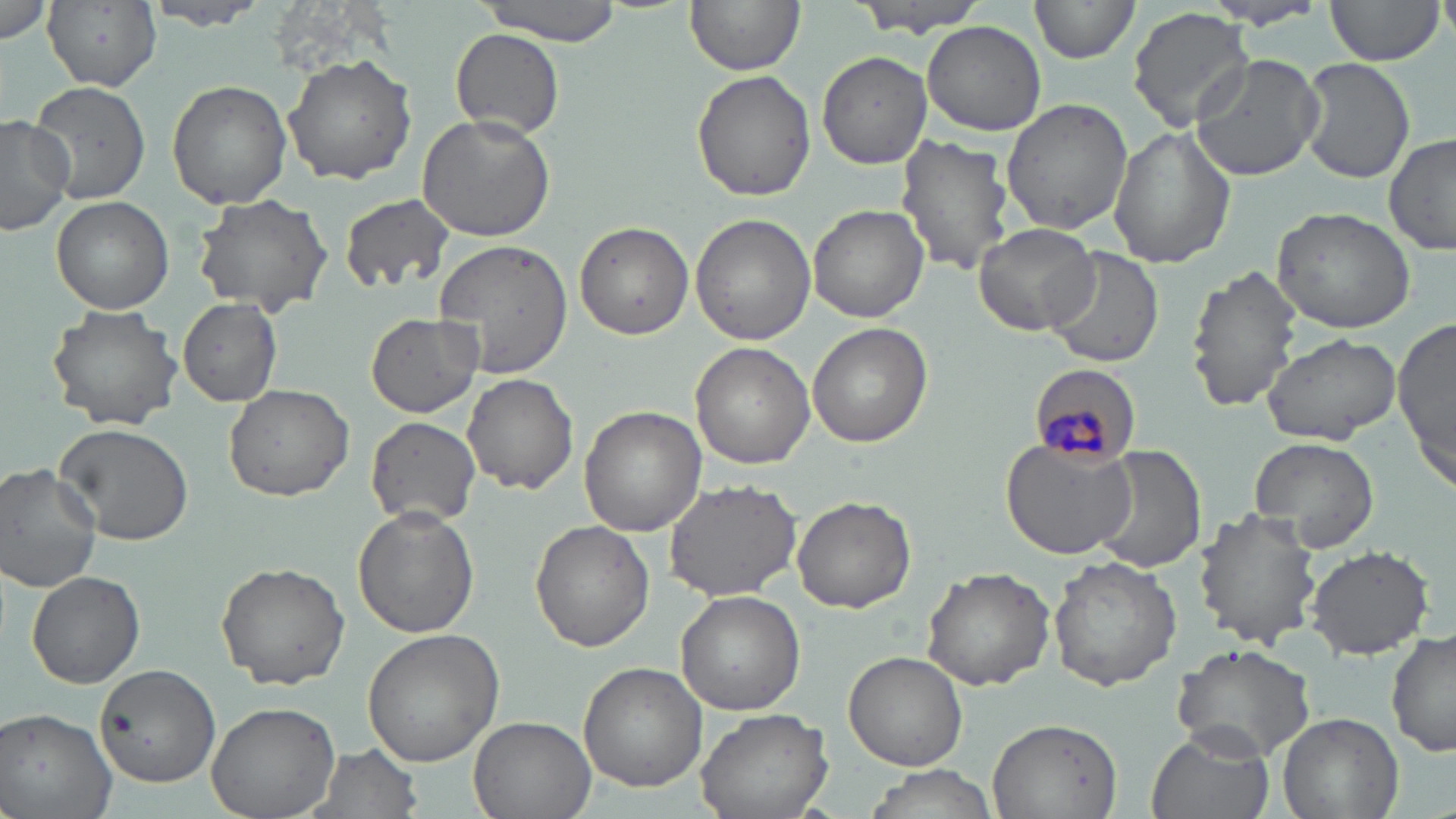
Summary:
  - Coordinate format: approximate bounding boxes as [x1, y1, x2, y2] in pixels
  - Plasmodium malariae-infected red blood cell locations: [1031, 365, 1143, 465]
  - Uninfected red blood cell locations: [144, 0, 266, 33], [476, 0, 625, 43], [683, 0, 803, 75], [850, 0, 990, 34], [1029, 0, 1139, 67], [0, 1, 57, 45], [44, 1, 164, 91], [1320, 1, 1446, 68], [1200, 2, 1331, 30], [1128, 6, 1254, 131], [922, 20, 1047, 135], [448, 29, 566, 137], [815, 51, 933, 170], [1189, 53, 1324, 182], [283, 54, 417, 184], [1297, 57, 1415, 183], [691, 69, 816, 199], [33, 76, 155, 205], [167, 79, 293, 210], [1000, 100, 1133, 233], [415, 113, 555, 243], [0, 116, 75, 236], [1107, 124, 1237, 267], [897, 134, 1020, 278], [1384, 134, 1456, 258], [191, 190, 335, 318], [339, 193, 455, 294], [50, 197, 174, 314], [807, 203, 929, 323], [1269, 206, 1416, 335], [691, 214, 814, 346], [574, 221, 693, 339], [973, 222, 1099, 335], [434, 237, 573, 379], [1045, 248, 1164, 370], [1185, 263, 1302, 414], [177, 298, 284, 406], [47, 304, 183, 430], [365, 312, 486, 417], [1393, 317, 1455, 488], [807, 321, 930, 446], [1262, 331, 1401, 446], [690, 341, 816, 468], [463, 372, 580, 495], [223, 383, 354, 501], [579, 406, 707, 536], [365, 415, 483, 528], [53, 421, 194, 545], [1247, 435, 1382, 554], [999, 437, 1134, 560], [1088, 446, 1207, 575], [0, 463, 103, 592], [661, 478, 805, 605], [791, 496, 915, 613], [351, 508, 480, 637], [1195, 508, 1319, 650], [530, 520, 655, 652], [1303, 543, 1435, 660], [1048, 556, 1182, 691], [216, 562, 351, 689], [920, 565, 1058, 691], [25, 570, 145, 688], [676, 590, 806, 714], [361, 628, 504, 765], [1388, 629, 1455, 761], [1168, 642, 1318, 763], [843, 650, 967, 770], [93, 662, 222, 788], [578, 663, 707, 791], [206, 702, 341, 819], [0, 706, 117, 818], [695, 708, 833, 819], [1278, 710, 1403, 819], [468, 715, 597, 819], [987, 718, 1121, 817], [1146, 728, 1278, 819], [307, 742, 426, 819], [859, 767, 1004, 818]
  - Slide-level diagnosis: Plasmodium malariae
  - Modality: optical microscopy
  - Image size: 1456×819 pixels
  - Field of view: one of a larger specimen
  - Preparation: thin blood smear
  - Magnification: 1000x
  - Stain: May-Grünwald-Giemsa